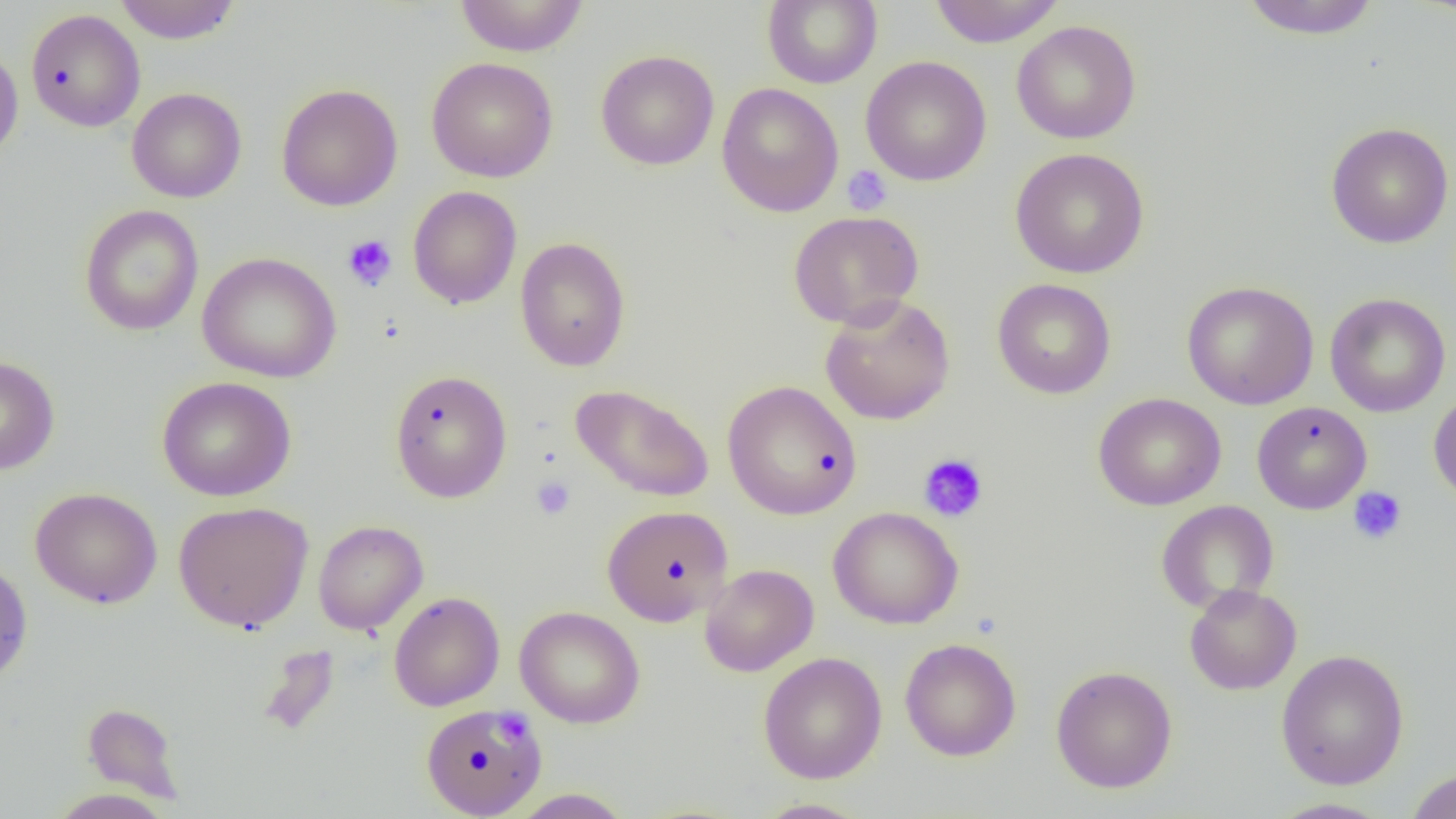
Summary:
  - Coordinate format: approximate bounding boxes as (x1, y1, x2, y2) in pixels
  - Platelet locations: (841, 165, 892, 215), (342, 234, 397, 291), (918, 452, 988, 522), (531, 476, 575, 520), (1348, 487, 1407, 545), (495, 712, 534, 754)
  - Uninfected red blood cell locations: (454, 0, 590, 57), (763, 0, 882, 89), (929, 0, 1065, 47), (1239, 0, 1382, 39), (113, 1, 242, 44), (26, 9, 145, 133), (1011, 20, 1141, 144), (0, 45, 24, 165), (596, 49, 719, 171), (426, 56, 558, 182), (861, 56, 991, 186), (716, 82, 844, 218), (275, 83, 403, 212), (126, 87, 247, 203), (1326, 122, 1454, 249), (1010, 148, 1149, 279), (407, 185, 522, 309), (79, 205, 204, 335), (788, 210, 924, 329), (515, 237, 631, 372), (197, 252, 341, 383), (992, 278, 1116, 399), (1181, 280, 1319, 410), (1324, 293, 1450, 417), (819, 294, 956, 426), (0, 355, 60, 475), (390, 368, 513, 503), (156, 376, 296, 501), (722, 380, 862, 521), (570, 383, 715, 503), (1428, 390, 1456, 505), (1093, 392, 1226, 511), (1252, 401, 1372, 514), (30, 487, 162, 609), (1156, 500, 1279, 615), (173, 501, 313, 632), (602, 505, 733, 627), (827, 506, 964, 629), (313, 520, 428, 635), (0, 558, 33, 685), (699, 563, 819, 677), (1184, 584, 1302, 695), (388, 591, 504, 712), (514, 605, 645, 728), (899, 638, 1022, 762), (258, 644, 341, 737), (1276, 649, 1409, 789), (758, 652, 887, 784), (1050, 665, 1178, 793), (82, 702, 184, 802), (421, 703, 547, 817), (1405, 768, 1456, 819), (509, 788, 633, 818), (48, 789, 175, 819), (753, 798, 871, 818), (1268, 798, 1397, 818)
  - Slide-level diagnosis: negative for blood parasites
  - Field of view: single
  - Modality: light microscopy
  - Image size: 1456×819 pixels
  - Preparation: thin blood film
  - Magnification: 1000x